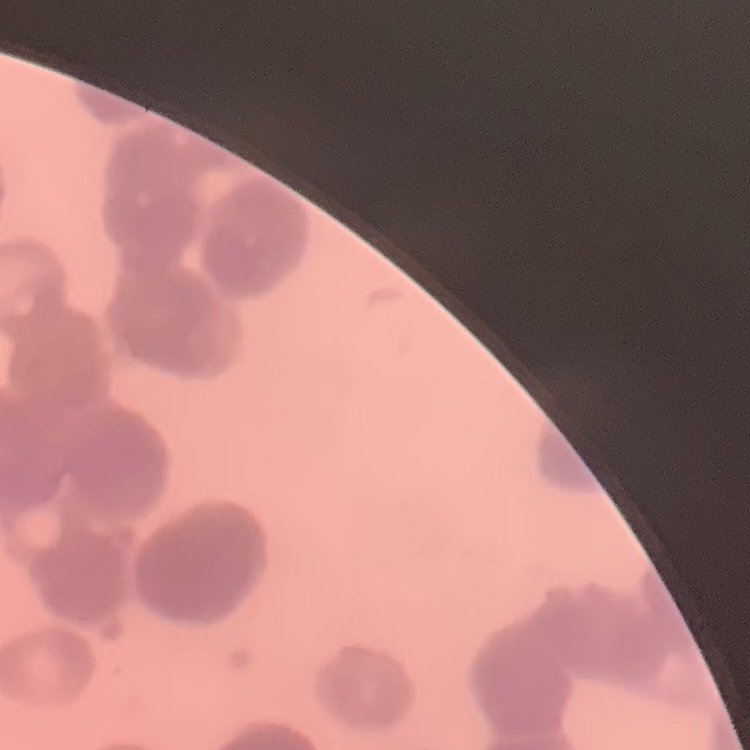

Summary:
  - Erythrocyte morphology: rouleaux formation
  - Preparation: thin peripheral smear
  - Image type: square crop of a larger photomicrograph
  - Stain: Field's or Giemsa